Comment on the morphology of the erythrocytes.
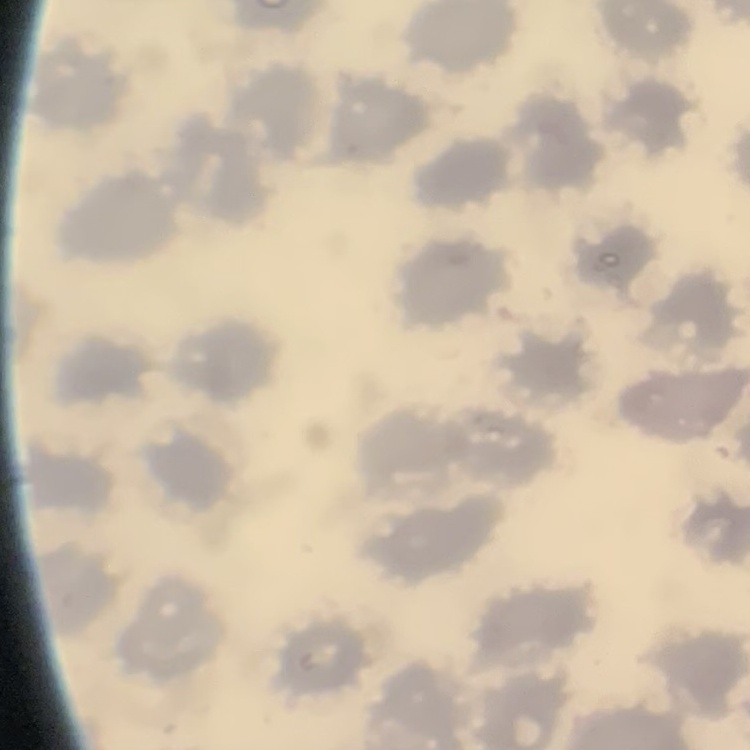

No rouleaux formation.

Thin blood smear. Square crop of a larger photomicrograph. Field's or Giemsa stain.